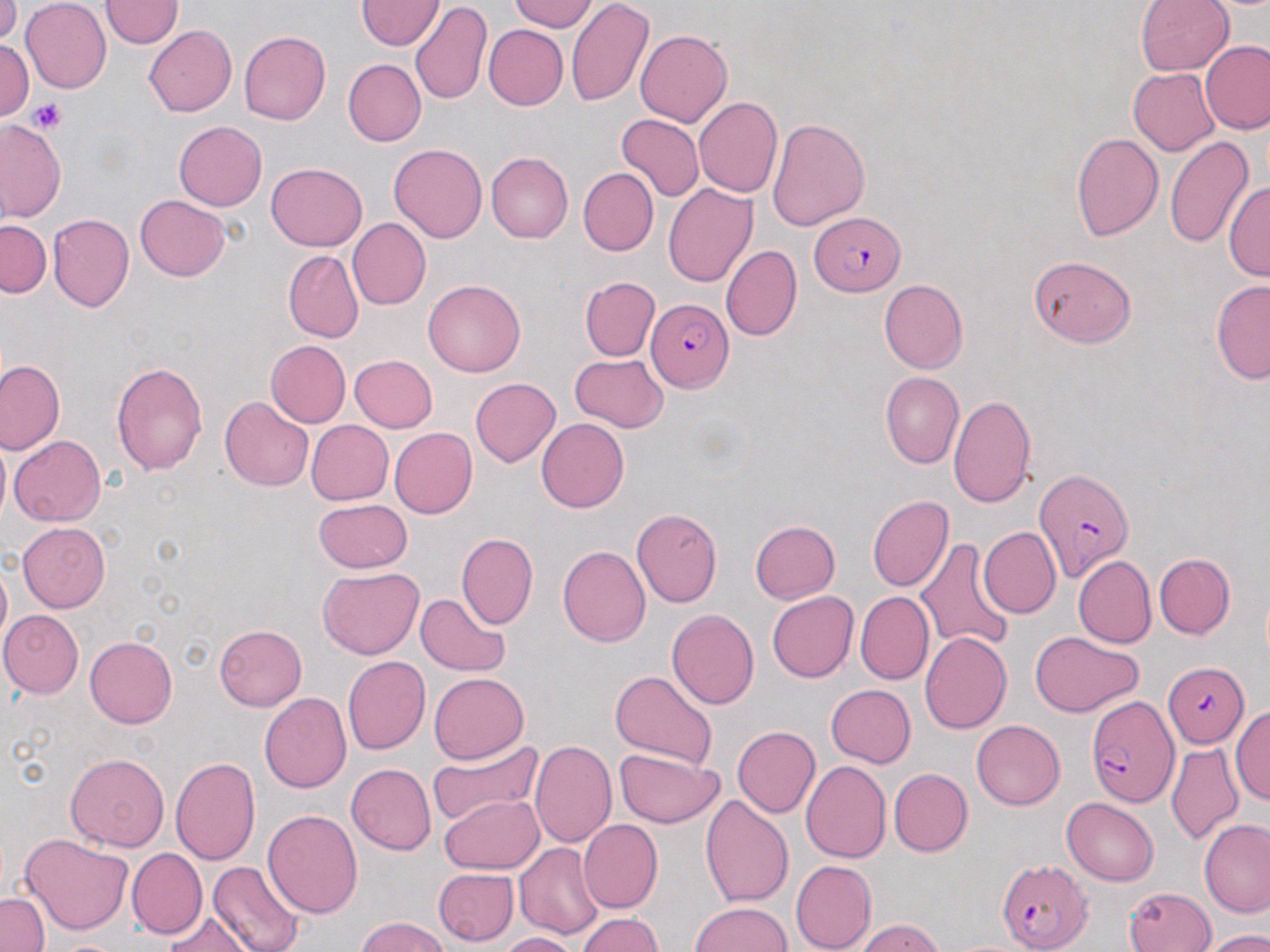 Approximate bounding boxes as [x1, y1, x2, y2] in pixels. Uninfected red blood cell locations: [104, 0, 179, 49], [507, 0, 598, 32], [566, 0, 654, 108], [1135, 0, 1234, 77], [21, 1, 112, 91], [360, 1, 443, 51], [0, 2, 21, 40], [410, 3, 491, 107], [142, 23, 236, 118], [485, 27, 568, 109], [635, 29, 734, 126], [239, 32, 331, 123], [0, 40, 35, 120], [1201, 42, 1270, 136], [345, 59, 426, 145], [1128, 69, 1219, 156], [693, 97, 781, 198], [615, 113, 703, 203], [766, 114, 870, 229], [3, 119, 65, 222], [174, 120, 269, 211], [1071, 133, 1164, 243], [1164, 135, 1253, 249], [388, 141, 486, 240], [486, 152, 573, 243], [266, 163, 369, 252], [577, 168, 656, 256], [1227, 179, 1269, 285], [661, 182, 756, 289], [135, 192, 230, 279], [46, 212, 135, 315], [347, 218, 431, 310], [0, 219, 50, 298], [720, 244, 801, 341], [283, 249, 364, 343], [1028, 254, 1135, 346], [580, 276, 658, 360], [880, 279, 968, 373], [1210, 279, 1270, 385], [422, 280, 527, 379], [266, 341, 350, 426], [348, 354, 437, 433], [569, 354, 669, 431], [0, 359, 63, 453], [111, 360, 211, 473], [882, 371, 965, 467], [469, 376, 562, 467], [948, 392, 1037, 510], [220, 397, 315, 492], [535, 418, 627, 513], [307, 420, 392, 503], [390, 427, 477, 518], [8, 435, 106, 526], [867, 494, 954, 592], [315, 496, 412, 573], [632, 509, 723, 610], [747, 518, 839, 605], [18, 522, 115, 612], [979, 527, 1061, 616], [458, 533, 538, 630], [918, 533, 1013, 654], [559, 545, 654, 647], [1155, 554, 1234, 638], [1073, 555, 1156, 647], [1, 559, 13, 650], [318, 567, 422, 658], [415, 591, 512, 678], [767, 591, 860, 683], [857, 592, 932, 683], [667, 608, 759, 710], [0, 610, 81, 696], [215, 622, 308, 709], [1029, 630, 1141, 717], [919, 631, 1009, 733], [85, 635, 178, 728], [341, 655, 431, 756], [607, 668, 716, 771], [429, 671, 529, 764], [825, 684, 916, 768], [261, 692, 352, 794], [1233, 703, 1270, 814], [971, 720, 1067, 810], [732, 724, 821, 819], [425, 736, 543, 831], [529, 740, 615, 846], [1164, 745, 1245, 842], [611, 748, 723, 829], [65, 751, 171, 851], [169, 754, 260, 865], [801, 760, 891, 863], [344, 764, 434, 855], [888, 768, 971, 856], [440, 793, 545, 872], [699, 793, 793, 907], [1061, 798, 1160, 885], [263, 808, 364, 918], [1200, 818, 1270, 920], [581, 820, 663, 912], [21, 832, 132, 934], [514, 842, 604, 939], [127, 848, 207, 938], [790, 859, 875, 951], [206, 863, 304, 952], [434, 868, 519, 944], [1124, 888, 1216, 952], [0, 891, 49, 952], [690, 900, 793, 952], [575, 912, 663, 952], [162, 913, 255, 952], [353, 918, 455, 952], [852, 918, 946, 952], [1202, 930, 1270, 951], [496, 932, 576, 952], [50, 935, 129, 951]. Plasmodium falciparum-infected red blood cell locations: [809, 213, 910, 296], [646, 299, 733, 393], [1035, 465, 1134, 582], [1163, 661, 1250, 748], [1083, 696, 1181, 806], [995, 856, 1090, 949]. Platelet locations: [29, 98, 66, 133]. Slide-level diagnosis: Plasmodium falciparum. 1000x magnification. Light microscopy. One field of a larger specimen. May-Grünwald-Giemsa stain. Image is 1270×952 pixels. Thin blood smear.